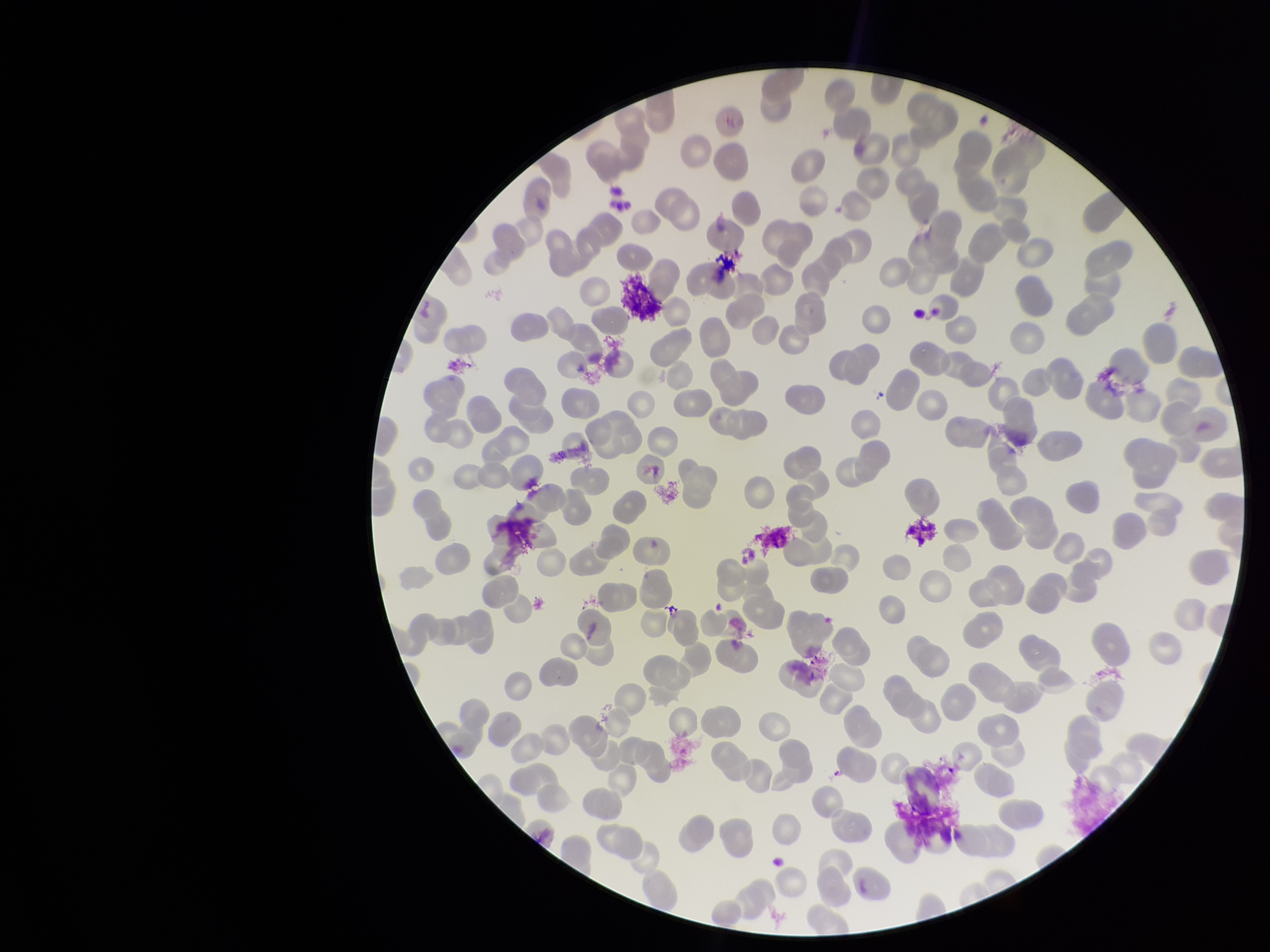

field of view = single
red blood cell count = 267
preparation = thin blood smear
parasitized red blood cell count = 0
parasitized red blood cells = none identified
stain = Giemsa
patient malaria status = negative
image size = 1270×952 pixels
capture = smartphone photograph through the microscope eyepiece